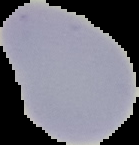

Summary:
  - Image type: cell region segmented out of the field of view; surrounding area masked to black
  - Preparation: thin blood smear
  - Image size: 139×145 pixels
  - Malaria status: uninfected